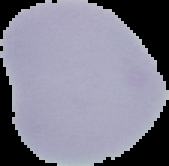
Image is 169×166 pixels. Segmented cell region on a black background. From a thin blood film. Malaria status: uninfected.